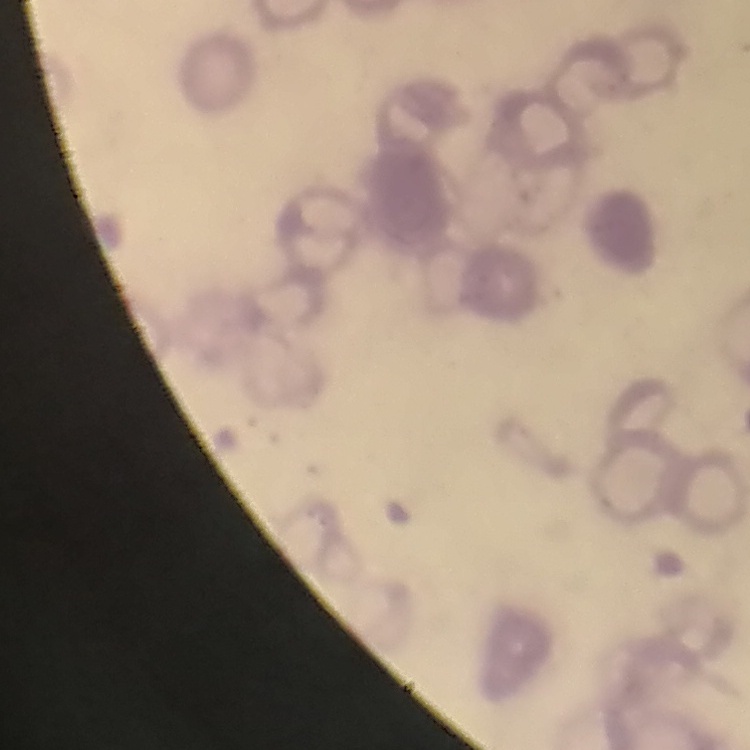
The red blood cells exhibit rouleaux formation. Stained with either Field's or Giemsa. One tile cut from a larger photomicrograph. Thin peripheral smear.